Comment on the morphology of the erythrocytes.
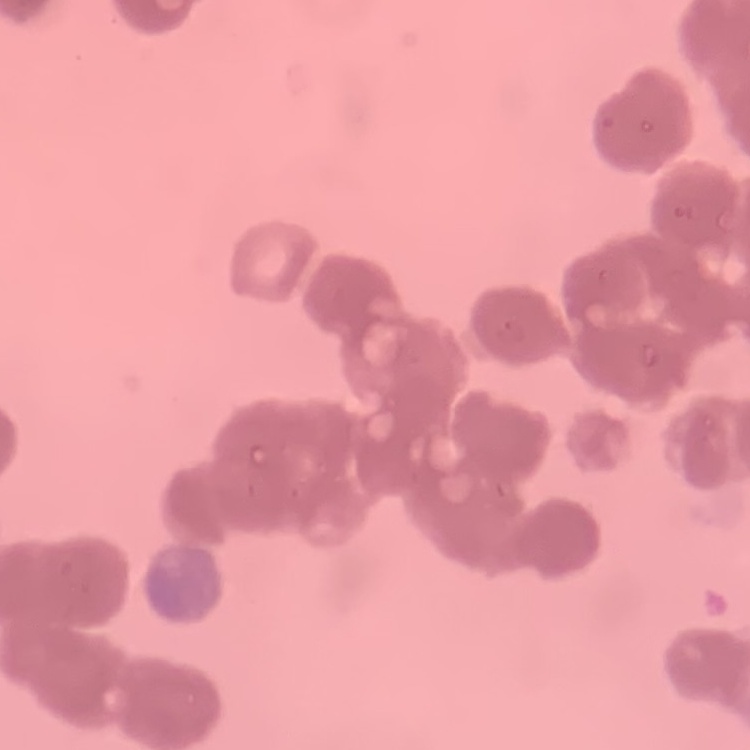
Rouleaux formation.

Field's or Giemsa stain. Thin blood smear. One tile cut from a larger photomicrograph.